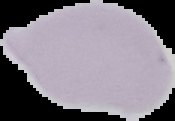

Image is 175×121 pixels. Malaria status: uninfected. The area outside the segmented cell region is set to black. From a thin blood smear.